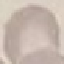

Summary:
  - Result: no malaria parasites detected
  - Image type: automatically extracted cell patch, resized to 64 × 64 pixels
  - Capture: smartphone camera at the microscope eyepiece
  - Preparation: thin blood smear
  - Stain: Giemsa